Locate every blood parasite and identify its species.
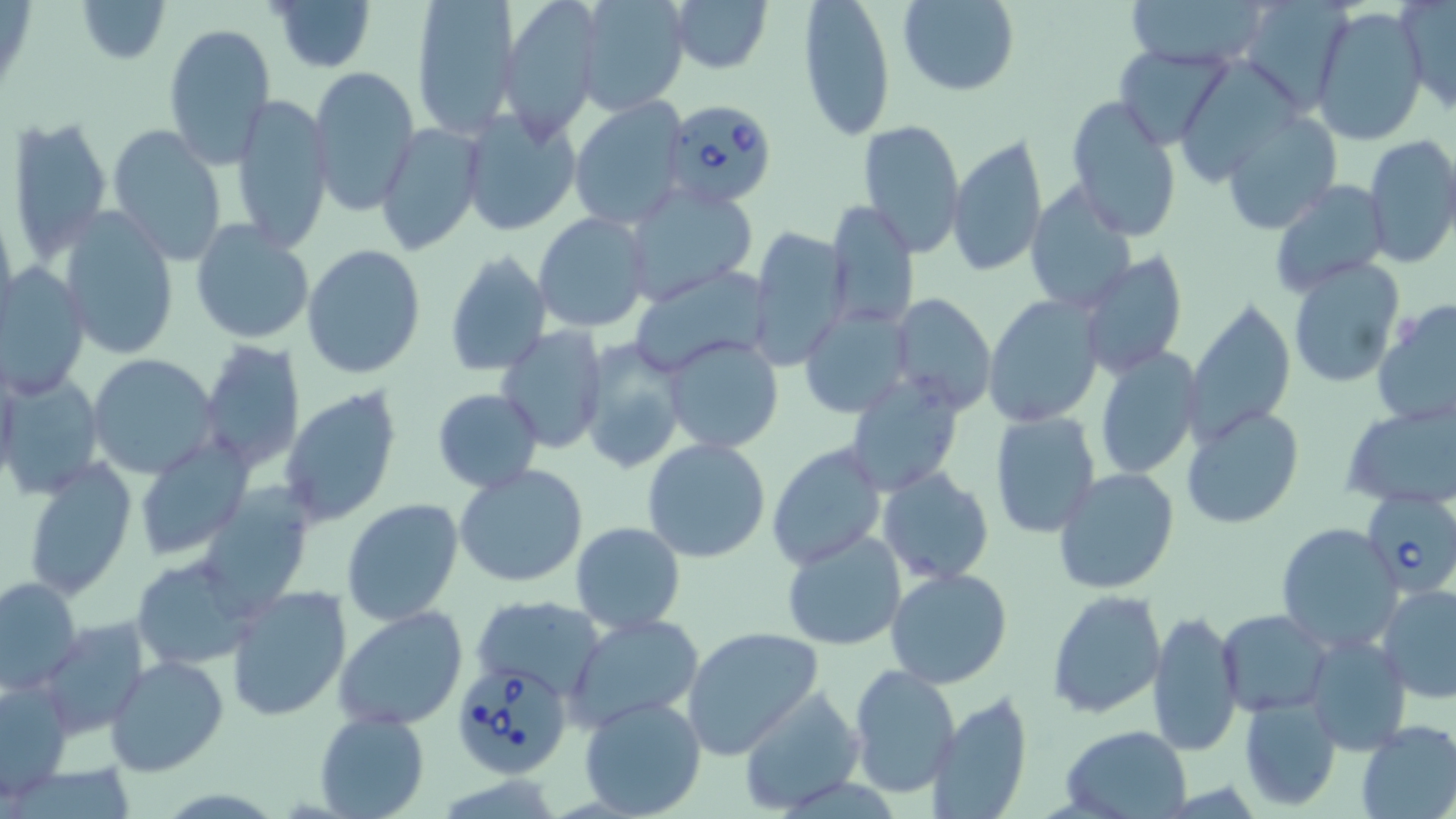
Approximate bounding boxes as named x1/y1/x2/y2 corners in pixels.
Babesia divergens-infected red blood cells: (x1=662, y1=98, x2=779, y2=207), (x1=1360, y1=489, x2=1456, y2=599), (x1=451, y1=657, x2=574, y2=778).
No Plasmodium falciparum, Plasmodium ovale, Plasmodium malariae, Plasmodium vivax, or Trypanosoma brucei observed.

Summary:
  - Uninfected red blood cell locations: (x1=75, y1=0, x2=170, y2=64), (x1=270, y1=0, x2=376, y2=73), (x1=410, y1=0, x2=520, y2=139), (x1=500, y1=0, x2=604, y2=136), (x1=575, y1=0, x2=690, y2=115), (x1=798, y1=0, x2=896, y2=142), (x1=897, y1=0, x2=1020, y2=95), (x1=1121, y1=0, x2=1270, y2=70), (x1=1239, y1=0, x2=1352, y2=112), (x1=1398, y1=0, x2=1456, y2=114), (x1=668, y1=1, x2=772, y2=74), (x1=1311, y1=6, x2=1429, y2=147), (x1=163, y1=22, x2=276, y2=167), (x1=1116, y1=45, x2=1233, y2=149), (x1=1173, y1=59, x2=1306, y2=185), (x1=306, y1=65, x2=419, y2=216), (x1=228, y1=93, x2=333, y2=253), (x1=1065, y1=96, x2=1183, y2=241), (x1=569, y1=97, x2=687, y2=229), (x1=458, y1=106, x2=583, y2=236), (x1=1221, y1=111, x2=1342, y2=236), (x1=6, y1=115, x2=114, y2=264), (x1=859, y1=118, x2=966, y2=257), (x1=375, y1=123, x2=484, y2=257), (x1=107, y1=125, x2=225, y2=265), (x1=947, y1=133, x2=1047, y2=278), (x1=1362, y1=135, x2=1456, y2=268), (x1=1266, y1=179, x2=1392, y2=299), (x1=623, y1=181, x2=759, y2=305), (x1=1023, y1=183, x2=1138, y2=314), (x1=825, y1=201, x2=919, y2=332), (x1=57, y1=206, x2=180, y2=360), (x1=534, y1=212, x2=649, y2=332), (x1=189, y1=221, x2=315, y2=346), (x1=746, y1=227, x2=848, y2=371), (x1=301, y1=244, x2=426, y2=379), (x1=443, y1=251, x2=551, y2=376), (x1=1080, y1=254, x2=1188, y2=378), (x1=1285, y1=256, x2=1405, y2=389), (x1=1, y1=264, x2=91, y2=399), (x1=628, y1=266, x2=774, y2=375), (x1=982, y1=292, x2=1105, y2=428), (x1=887, y1=293, x2=997, y2=413), (x1=1184, y1=299, x2=1295, y2=443), (x1=1372, y1=300, x2=1456, y2=430), (x1=798, y1=306, x2=913, y2=418), (x1=496, y1=327, x2=607, y2=452), (x1=660, y1=336, x2=784, y2=455), (x1=197, y1=338, x2=305, y2=476), (x1=578, y1=342, x2=687, y2=473), (x1=1094, y1=348, x2=1203, y2=480), (x1=88, y1=354, x2=218, y2=479), (x1=1, y1=372, x2=103, y2=499), (x1=841, y1=372, x2=964, y2=496), (x1=279, y1=387, x2=402, y2=528), (x1=431, y1=388, x2=544, y2=492), (x1=1340, y1=403, x2=1454, y2=511), (x1=1181, y1=405, x2=1305, y2=530), (x1=989, y1=410, x2=1101, y2=538), (x1=134, y1=435, x2=254, y2=561), (x1=643, y1=438, x2=771, y2=563), (x1=766, y1=441, x2=886, y2=570), (x1=21, y1=458, x2=136, y2=600), (x1=454, y1=463, x2=589, y2=588), (x1=878, y1=467, x2=994, y2=584), (x1=1054, y1=468, x2=1179, y2=594), (x1=860, y1=473, x2=1004, y2=673), (x1=341, y1=498, x2=465, y2=627), (x1=571, y1=521, x2=685, y2=634), (x1=1275, y1=523, x2=1403, y2=653), (x1=781, y1=531, x2=908, y2=650), (x1=128, y1=554, x2=260, y2=669), (x1=884, y1=566, x2=1013, y2=688), (x1=0, y1=577, x2=81, y2=695), (x1=1377, y1=582, x2=1456, y2=703), (x1=223, y1=585, x2=350, y2=722), (x1=1046, y1=590, x2=1166, y2=719), (x1=472, y1=596, x2=606, y2=699), (x1=333, y1=605, x2=468, y2=730), (x1=1217, y1=608, x2=1331, y2=715), (x1=1147, y1=609, x2=1244, y2=758), (x1=565, y1=613, x2=707, y2=736), (x1=40, y1=618, x2=150, y2=739), (x1=682, y1=626, x2=822, y2=758), (x1=1305, y1=631, x2=1411, y2=752), (x1=104, y1=654, x2=230, y2=777), (x1=847, y1=664, x2=958, y2=798), (x1=1, y1=680, x2=72, y2=801), (x1=736, y1=685, x2=865, y2=813), (x1=924, y1=690, x2=1035, y2=819), (x1=1239, y1=694, x2=1342, y2=812), (x1=577, y1=695, x2=708, y2=819), (x1=313, y1=711, x2=431, y2=819), (x1=1355, y1=720, x2=1456, y2=819), (x1=1056, y1=725, x2=1194, y2=817)
  - Slide-level diagnosis: Babesia divergens
  - Preparation: thin blood smear
  - Field of view: one of a larger specimen
  - Image size: 1456×819 pixels
  - Stain: May-Grünwald-Giemsa
  - Magnification: 1000x
  - Modality: light microscopy